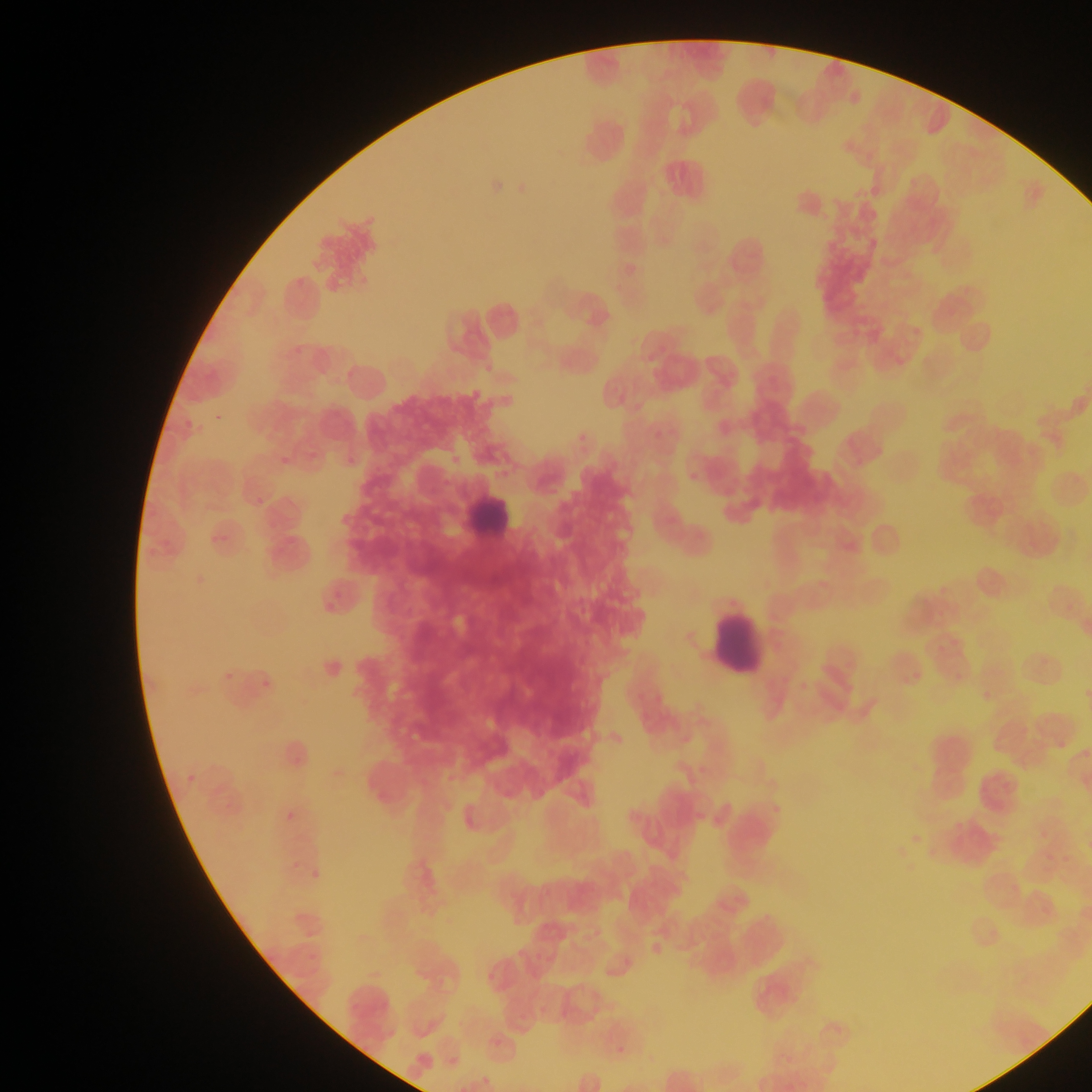
Approximate bounding boxes as (left, top, right, bottom) in pixels.
Summary:
  - Leukocyte locations: (462, 480, 517, 541), (710, 612, 772, 676)
  - Malaria parasite locations: (481, 364, 492, 372), (213, 417, 221, 426), (279, 459, 293, 470), (256, 494, 262, 506), (339, 515, 350, 524), (261, 678, 271, 689), (184, 768, 199, 785), (282, 807, 295, 818), (290, 862, 300, 874), (312, 869, 327, 883)
  - Country: Ghana
  - Field of view: single
  - Image size: 1092×1092 pixels
  - Capture: mobile-phone photograph through a microscope
  - Preparation: thin blood film